Comment on the morphology of the red blood cells.
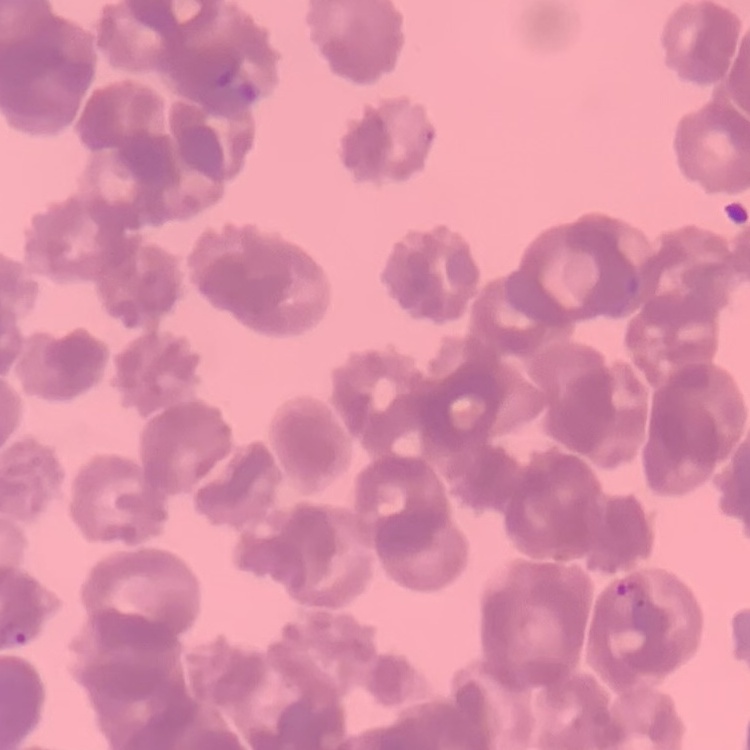

Rouleaux formation.

{
  "preparation": "thin blood smear",
  "image_type": "one tile cut from a larger photomicrograph",
  "stain": "Field's or Giemsa"
}